Comment on the morphology of the red blood cells.
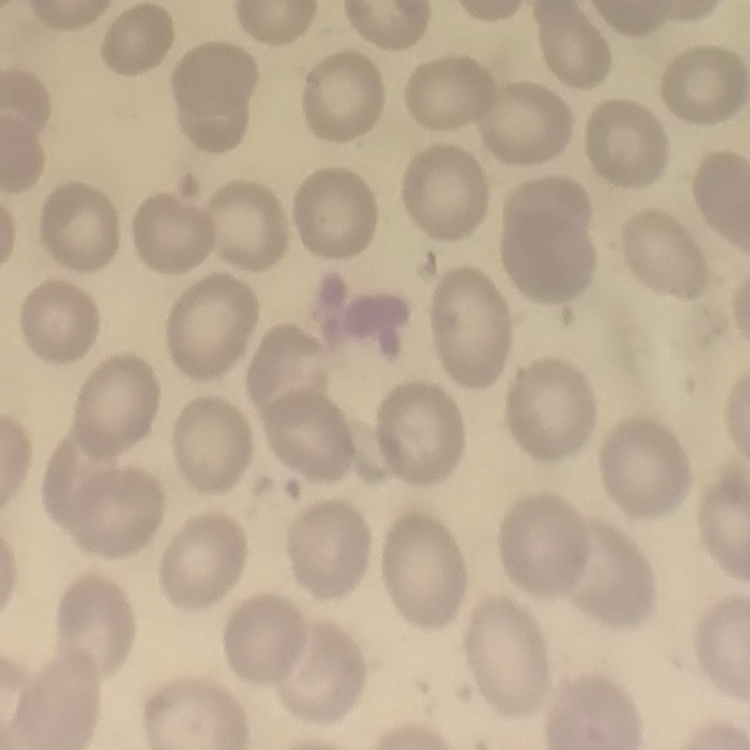

No rouleaux formation.

Thin blood smear. Field's or Giemsa stain. Square crop of a larger photomicrograph.